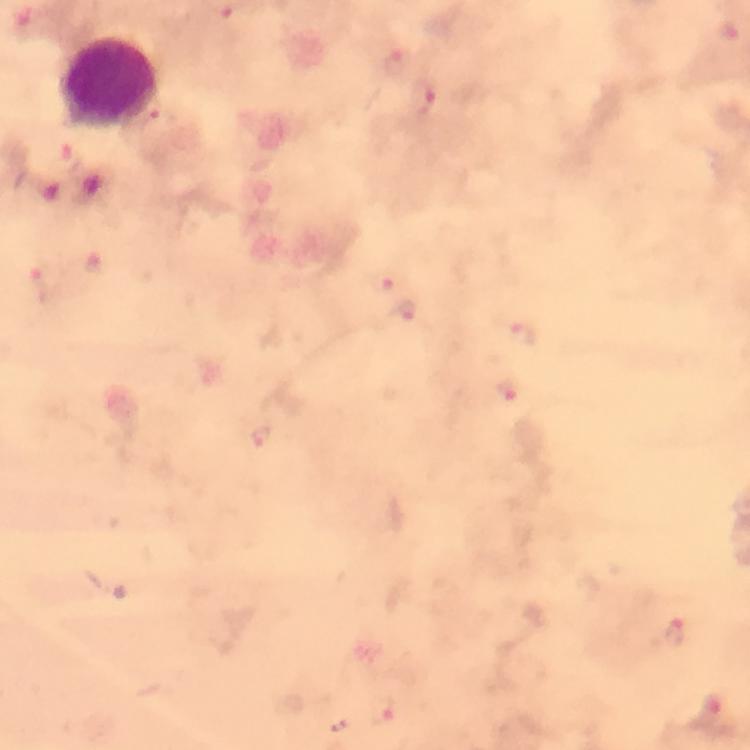
Approximate centers as [x, y] in pixels.
Summary:
  - Plasmodium parasite locations: [396, 61], [422, 103], [388, 279], [48, 280], [406, 314], [529, 339], [509, 393], [261, 437], [675, 632], [383, 711], [711, 716]
  - Leukocyte locations: [108, 83]
  - Immersion oil: used
  - Preparation: thick blood smear
  - Cropped from: a single field of view
  - Magnification: 100x
  - Capture: smartphone photograph through a microscope
  - Stain: Giemsa
  - Context: from a malaria diagnostic workup
  - Image size: 750×750 pixels